Outline every parasitised red blood cell.
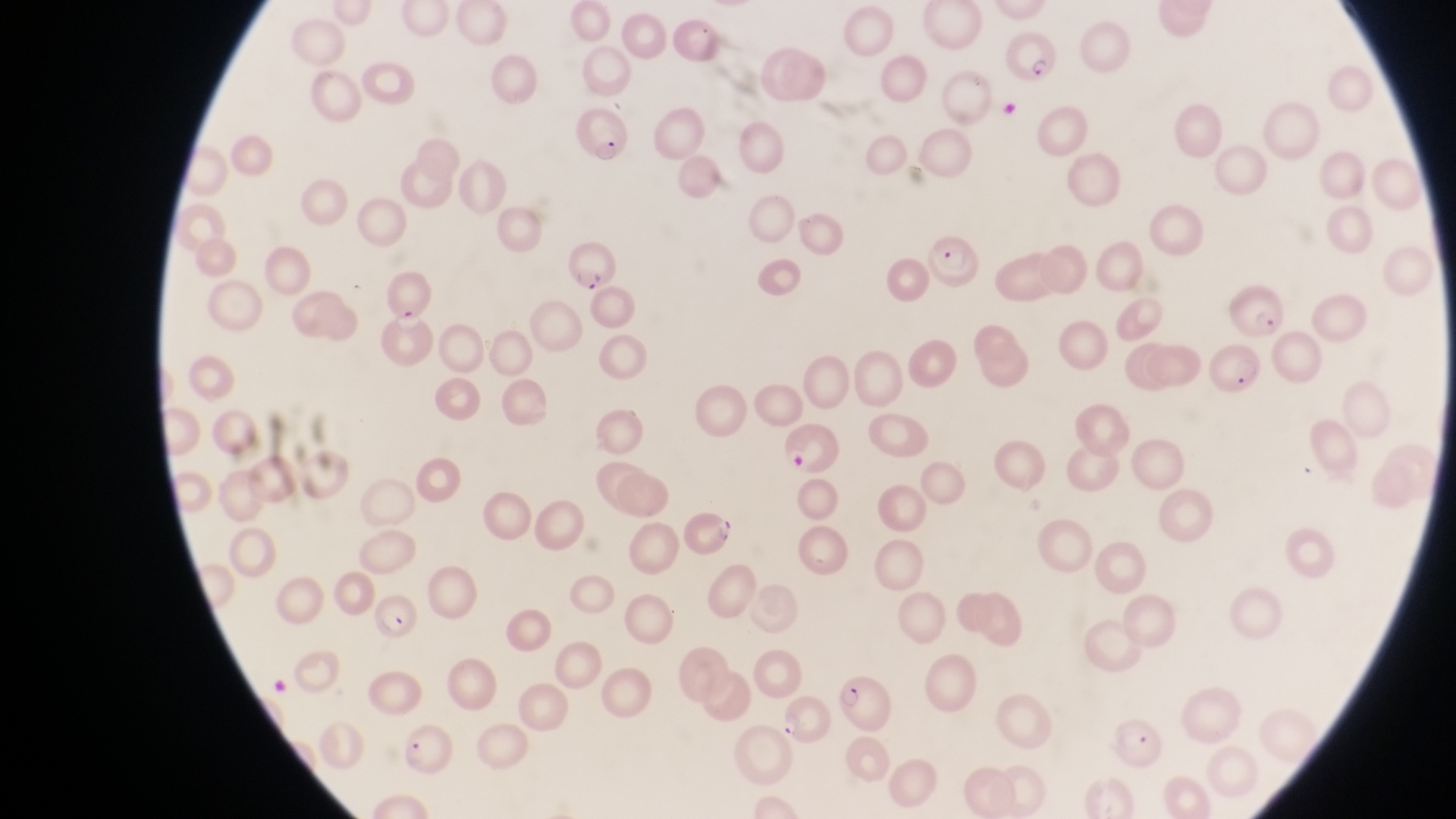
Approximate bounding boxes as (left, top, right, bottom) in pixels.
Parasitised red blood cells: (1003, 29, 1058, 87), (573, 106, 634, 167), (927, 231, 985, 289), (563, 238, 621, 296), (1231, 280, 1287, 339), (363, 303, 432, 376), (1208, 344, 1267, 399), (686, 510, 738, 559), (369, 589, 422, 635), (836, 671, 895, 737), (782, 695, 831, 751), (1112, 713, 1164, 768), (403, 724, 456, 774).

{
  "preparation": "thin blood film",
  "artifact_platelet_like_body_stain_precipitate_or_debris_locations": "approximate bounding boxes as (left, top, right, bottom) in pixels: (782, 446, 815, 473)",
  "magnification": "1000x",
  "image_size": "1456×819 pixels",
  "country": "Uganda",
  "capture": "smartphone photograph through the eyepiece of an Olympus CX-23 microscope",
  "field_of_view": "single"
}